State the blood parasite species.
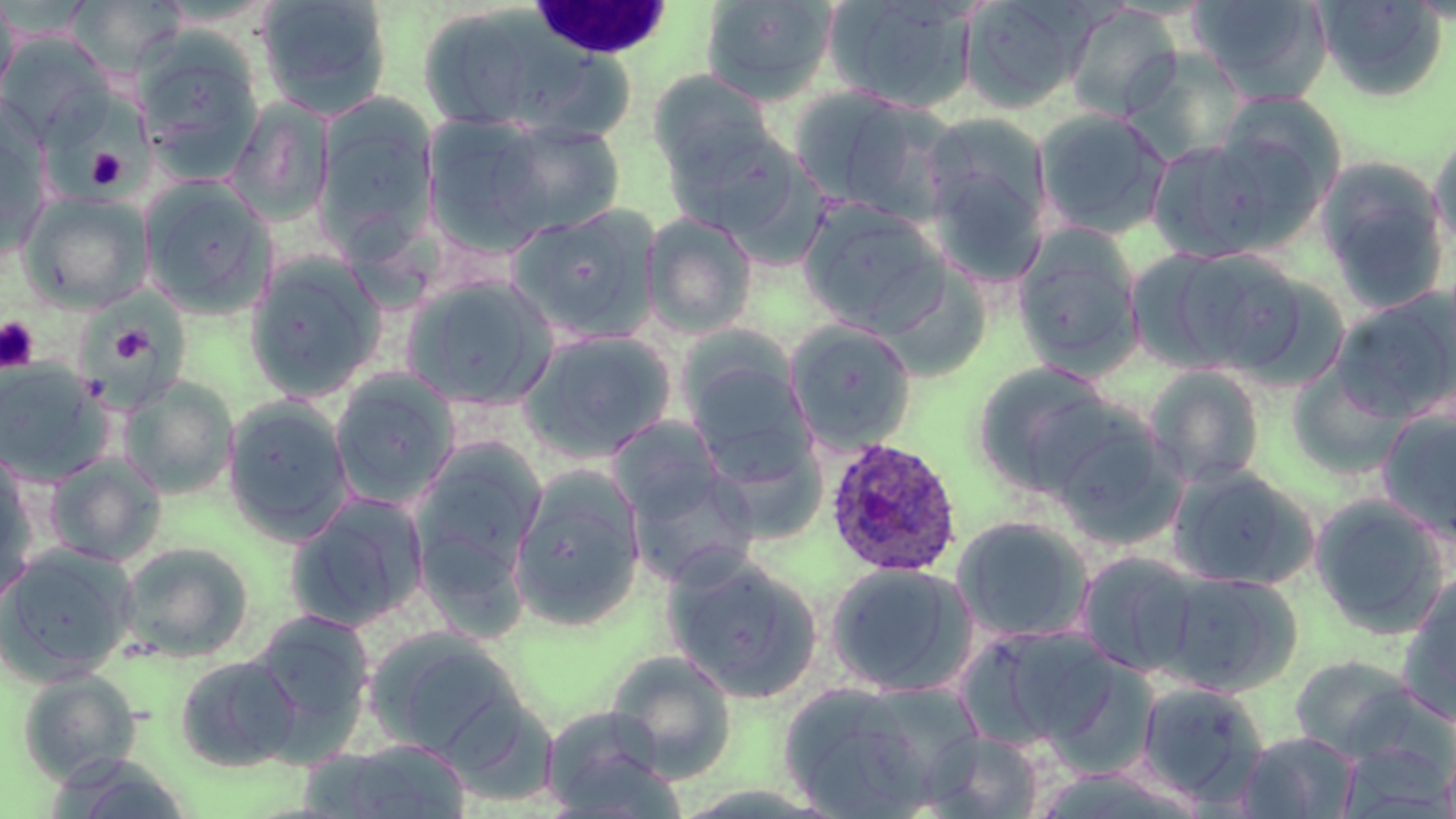

Plasmodium ovale.

Summary:
  - Coordinate format: approximate bounding boxes as [x1, y1, x2, y2] in pixels
  - White blood cell locations: [531, 0, 677, 65]
  - Platelet locations: [86, 148, 128, 189], [0, 316, 40, 374], [115, 330, 162, 368]
  - Uninfected red blood cell locations: [0, 0, 21, 108], [256, 0, 393, 120], [699, 0, 839, 104], [823, 0, 980, 115], [960, 0, 1092, 113], [1188, 0, 1331, 99], [1314, 0, 1448, 100], [67, 1, 187, 76], [1065, 4, 1182, 122], [416, 6, 597, 135], [0, 34, 114, 145], [133, 35, 264, 174], [1121, 47, 1248, 164], [647, 71, 777, 180], [790, 87, 961, 224], [1214, 92, 1346, 205], [224, 98, 335, 226], [317, 105, 436, 247], [1034, 108, 1172, 240], [921, 111, 1052, 279], [456, 117, 629, 246], [663, 122, 808, 242], [1428, 126, 1456, 257], [0, 129, 51, 259], [1147, 135, 1287, 263], [1316, 157, 1451, 314], [139, 177, 278, 318], [20, 190, 153, 312], [797, 198, 951, 335], [509, 205, 660, 342], [641, 211, 758, 338], [1011, 224, 1145, 377], [1136, 245, 1311, 378], [244, 253, 386, 403], [404, 274, 559, 411], [1329, 290, 1456, 424], [75, 295, 186, 408], [785, 320, 917, 454], [517, 328, 677, 464], [682, 350, 815, 481], [0, 359, 111, 485], [971, 362, 1128, 500], [1145, 365, 1266, 488], [330, 370, 460, 509], [120, 376, 238, 499], [222, 396, 355, 543], [1377, 407, 1456, 543], [1045, 409, 1186, 548], [609, 416, 729, 528], [410, 439, 546, 594], [44, 453, 166, 567], [0, 456, 38, 610], [624, 457, 759, 590], [1167, 465, 1318, 591], [508, 466, 646, 631], [284, 494, 429, 633], [1309, 494, 1450, 639], [951, 515, 1096, 644], [118, 541, 254, 662], [1, 545, 136, 683], [1074, 551, 1204, 678], [662, 555, 824, 703], [824, 562, 978, 699], [1161, 570, 1303, 696], [1401, 574, 1456, 717], [245, 610, 376, 756], [966, 623, 1119, 750], [366, 629, 526, 760], [604, 649, 738, 782], [173, 654, 302, 773], [1290, 654, 1424, 761], [16, 669, 142, 785], [777, 681, 948, 818], [1135, 681, 1269, 806], [538, 705, 680, 817], [919, 729, 1045, 817], [1237, 730, 1361, 818], [316, 738, 475, 818]
  - Plasmodium ovale-infected red blood cell locations: [824, 437, 964, 578]
  - Field of view: one of a larger specimen
  - Preparation: thin blood smear
  - Magnification: 1000x
  - Image size: 1456×819 pixels
  - Stain: May-Grünwald-Giemsa
  - Modality: light microscopy